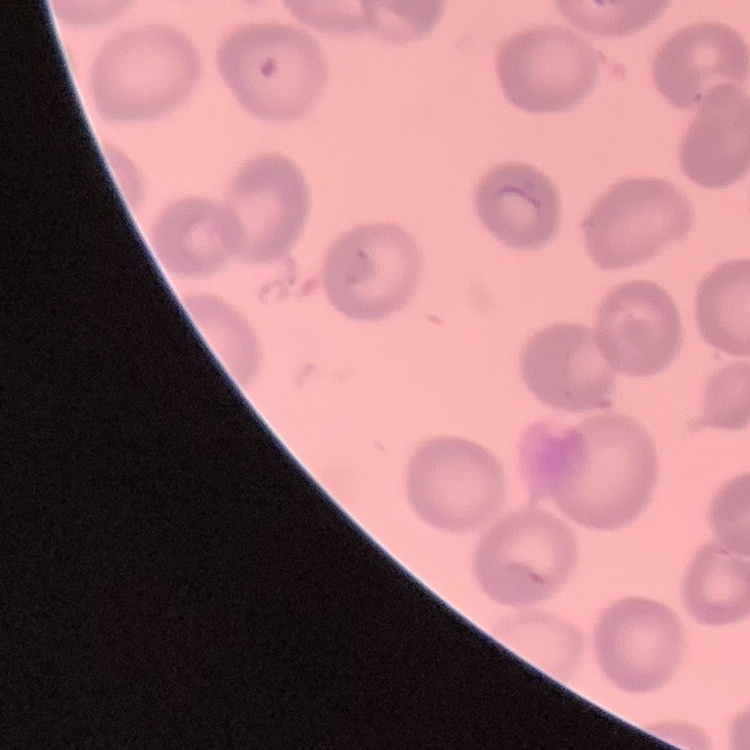
{
  "red_blood_cell_morphology": "no rouleaux formation",
  "stain": "Field's or Giemsa",
  "preparation": "thin blood film",
  "image_type": "square crop of a larger photomicrograph"
}